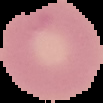

image_size: 103×103 pixels
malaria_status: uninfected
image_type: cell region segmented out of the field of view; surrounding area masked to black
preparation: thin blood smear